Give the extent of all Plasmodium falciparum-infected red blood cells.
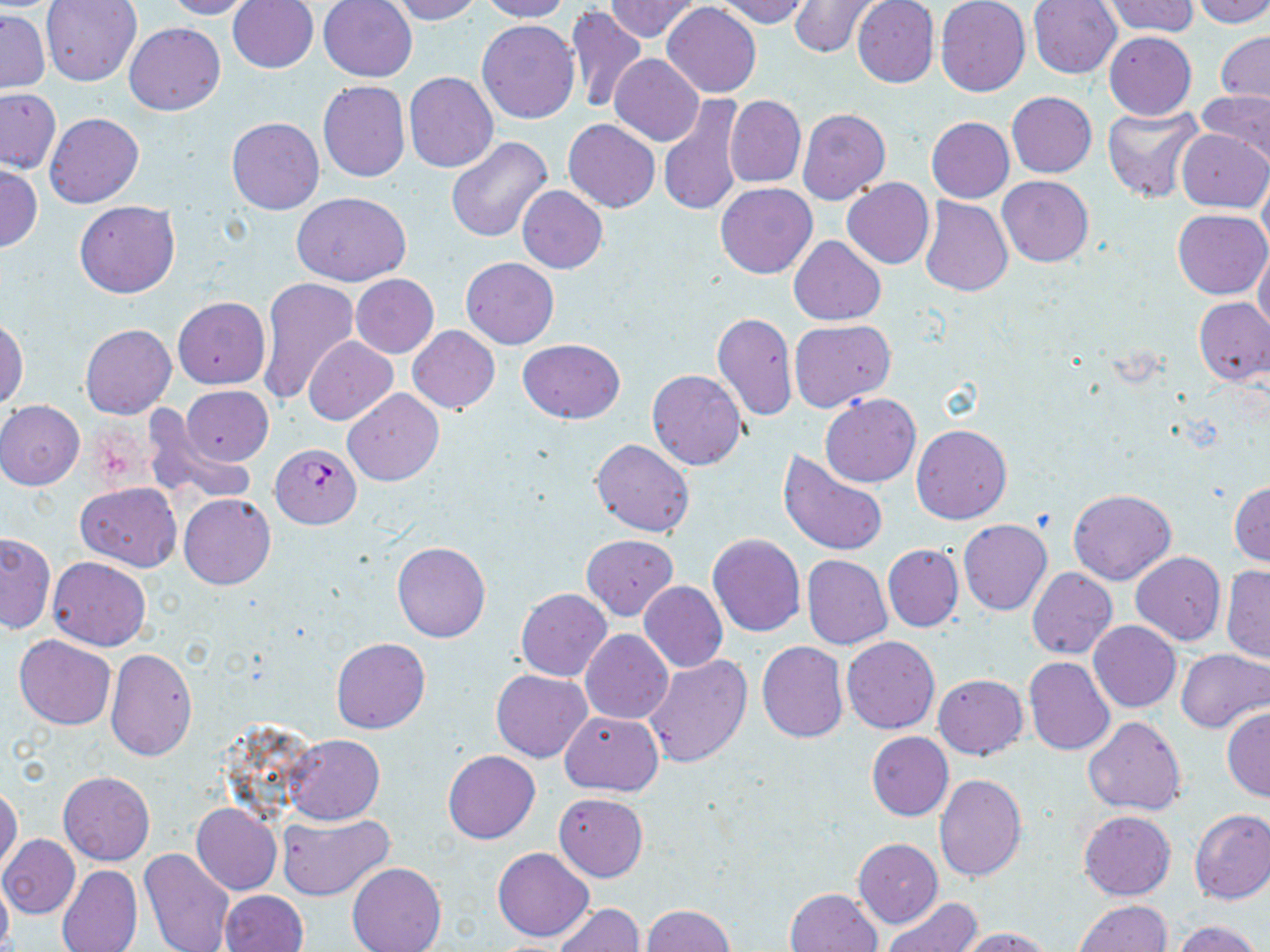
Approximate bounding boxes as (x1, y1, x2, y2) in pixels.
Plasmodium falciparum-infected red blood cells: (270, 442, 362, 529).

slide-level diagnosis = Plasmodium falciparum
uninfected red blood cell locations = approximate bounding boxes as (x1, y1, x2, y2) in pixels: (41, 0, 142, 86), (162, 0, 258, 20), (389, 0, 485, 23), (479, 0, 570, 22), (713, 0, 812, 27), (935, 0, 1030, 97), (1028, 0, 1122, 78), (1101, 0, 1200, 37), (1189, 0, 1270, 27), (228, 1, 318, 73), (318, 1, 418, 82), (604, 1, 701, 41), (787, 1, 878, 58), (851, 1, 939, 88), (662, 2, 761, 98), (566, 7, 648, 114), (1, 10, 50, 93), (477, 20, 579, 124), (124, 22, 225, 115), (1103, 31, 1197, 120), (1217, 31, 1270, 107), (610, 53, 703, 146), (404, 72, 497, 172), (318, 80, 410, 182), (0, 89, 61, 175), (1196, 90, 1270, 167), (1006, 91, 1097, 177), (658, 94, 746, 217), (725, 96, 805, 188), (1101, 105, 1204, 203), (798, 109, 890, 205), (44, 112, 145, 209), (926, 116, 1014, 202), (226, 117, 323, 215), (563, 119, 660, 212), (1177, 129, 1269, 212), (445, 136, 553, 244), (0, 166, 42, 253), (1259, 172, 1270, 258), (997, 175, 1093, 265), (842, 178, 934, 269), (715, 182, 816, 279), (517, 186, 607, 273), (290, 191, 411, 286), (918, 197, 1014, 296), (74, 200, 179, 298), (1173, 209, 1270, 299), (790, 235, 885, 325), (1254, 247, 1270, 340), (461, 257, 558, 349), (350, 275, 439, 357), (256, 277, 358, 406), (172, 298, 270, 389), (1193, 298, 1269, 386), (712, 311, 796, 424), (0, 317, 28, 410), (790, 319, 895, 412), (80, 324, 176, 419), (407, 326, 500, 413), (304, 337, 398, 424), (516, 339, 628, 420), (646, 369, 747, 470), (181, 385, 274, 465), (343, 388, 443, 486), (820, 394, 921, 487), (0, 400, 84, 489), (146, 412, 256, 507), (911, 424, 1012, 523), (590, 439, 695, 537), (778, 450, 888, 557), (76, 481, 181, 572), (1229, 481, 1270, 566), (1067, 487, 1175, 584), (179, 494, 275, 590), (959, 520, 1051, 616), (0, 532, 55, 634), (708, 533, 805, 637), (581, 534, 678, 619), (392, 541, 491, 642), (883, 544, 964, 632), (1131, 552, 1226, 645), (802, 554, 892, 649), (48, 556, 150, 650), (1221, 565, 1270, 664), (1027, 566, 1117, 660), (639, 581, 728, 673), (516, 588, 612, 681), (1089, 620, 1181, 712), (581, 630, 673, 725), (14, 635, 116, 730), (841, 636, 940, 734), (331, 637, 430, 734), (757, 641, 848, 743), (1175, 648, 1270, 733), (104, 649, 197, 761), (642, 653, 753, 767), (1024, 657, 1114, 755), (492, 670, 591, 762), (933, 673, 1027, 759), (1222, 707, 1270, 803), (559, 710, 663, 796), (1084, 716, 1187, 816), (865, 731, 953, 821), (284, 733, 384, 825), (443, 750, 540, 844), (59, 771, 154, 866), (933, 775, 1028, 882), (0, 784, 23, 876), (554, 792, 648, 881), (192, 804, 281, 894), (1189, 808, 1270, 904), (1078, 810, 1176, 900), (277, 812, 394, 901), (0, 834, 79, 919), (853, 838, 943, 927), (493, 847, 593, 941), (139, 848, 235, 952), (347, 861, 446, 952), (58, 864, 142, 952), (0, 874, 13, 952), (786, 888, 882, 952), (220, 891, 308, 952), (880, 898, 981, 952), (1073, 900, 1171, 952), (554, 903, 645, 951), (643, 904, 733, 952), (1168, 920, 1265, 952), (957, 926, 1058, 952)
preparation = thin blood film
magnification = 1000x
field of view = one of a larger specimen
modality = light microscopy
stain = May-Grünwald-Giemsa
image size = 1270×952 pixels